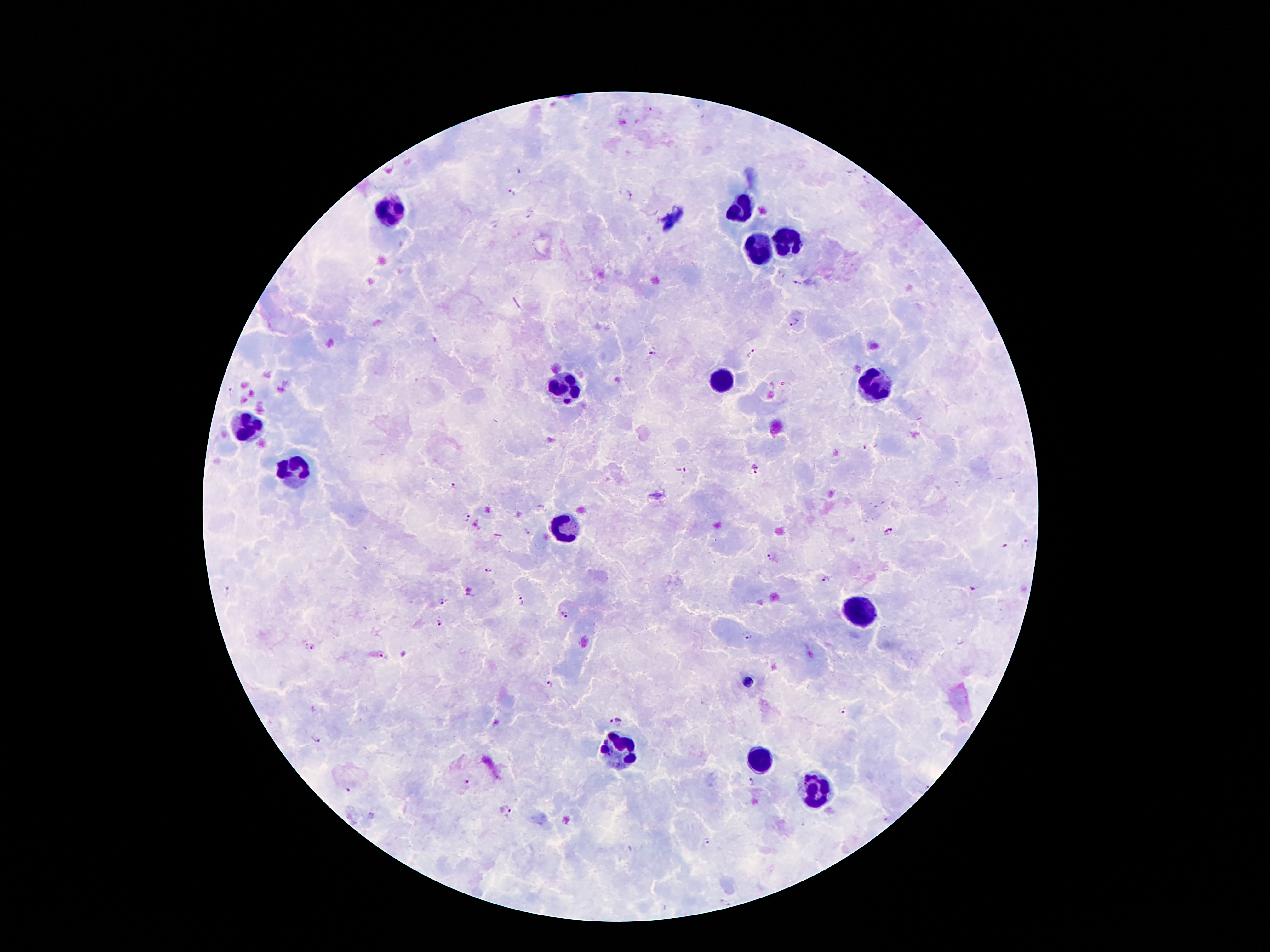

{
  "stain": "Giemsa",
  "leukocyte_locations": "approximate centers as (x, y) in pixels: (395, 207), (740, 211), (789, 242), (762, 249), (873, 382), (722, 383), (565, 385), (249, 425), (294, 469), (566, 530), (860, 611), (618, 751), (759, 760), (817, 788)",
  "field_of_view": "single",
  "malaria_parasite_locations": "approximate centers as (x, y) in pixels: (650, 108), (519, 172), (868, 182), (510, 193), (630, 194), (530, 215), (495, 224), (799, 283), (794, 324), (652, 351), (753, 353), (230, 392), (866, 448), (754, 470), (681, 471), (452, 486), (466, 518), (526, 530), (889, 532), (1028, 543), (1005, 545), (770, 556), (488, 571), (827, 580), (974, 587), (470, 589), (228, 592), (469, 597), (522, 601), (443, 603), (565, 615), (438, 623), (747, 636), (310, 647), (383, 656), (551, 683), (843, 711), (616, 721), (315, 738), (467, 782), (752, 783), (349, 790), (509, 813), (886, 820), (708, 842)",
  "preparation": "thick blood film",
  "capture": "smartphone through the microscope eyepiece",
  "magnification": "100x",
  "patient_malaria_status": "infected with Plasmodium falciparum",
  "image_size": "1270×952 pixels"
}